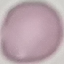

malaria status = uninfected
stain = Giemsa
capture = smartphone camera at the microscope eyepiece
preparation = thin blood film
image type = automatically extracted cell patch, resized to 64 × 64 pixels